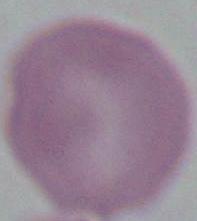

Summary:
  - Identification: red blood cell
  - Modality: micrograph
  - Magnification: 1000x